Classify this cell by malaria status.
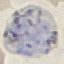
It is parasitized.

Cell patch, automatically extracted from a larger field of view and resized to 64 × 64 pixels. Photographed with a smartphone camera at the microscope eyepiece. Thin blood film. Giemsa-stained preparation.